Name the parasite shown.
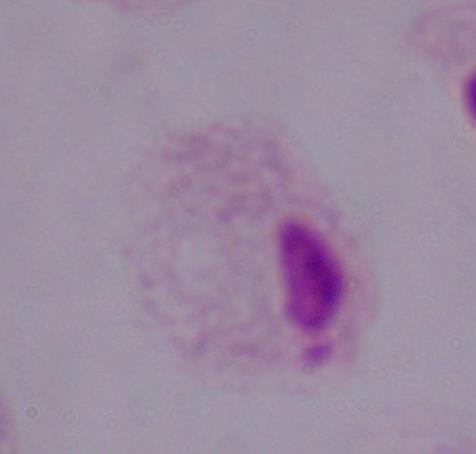
A trichomonad.

Summary:
  - Magnification: 1000x
  - Modality: micrograph